Report the malaria status of this cell.
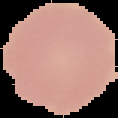
It is uninfected.

Summary:
  - Preparation: thin blood smear
  - Image size: 118×118 pixels
  - Image type: segmented cell region on a black background